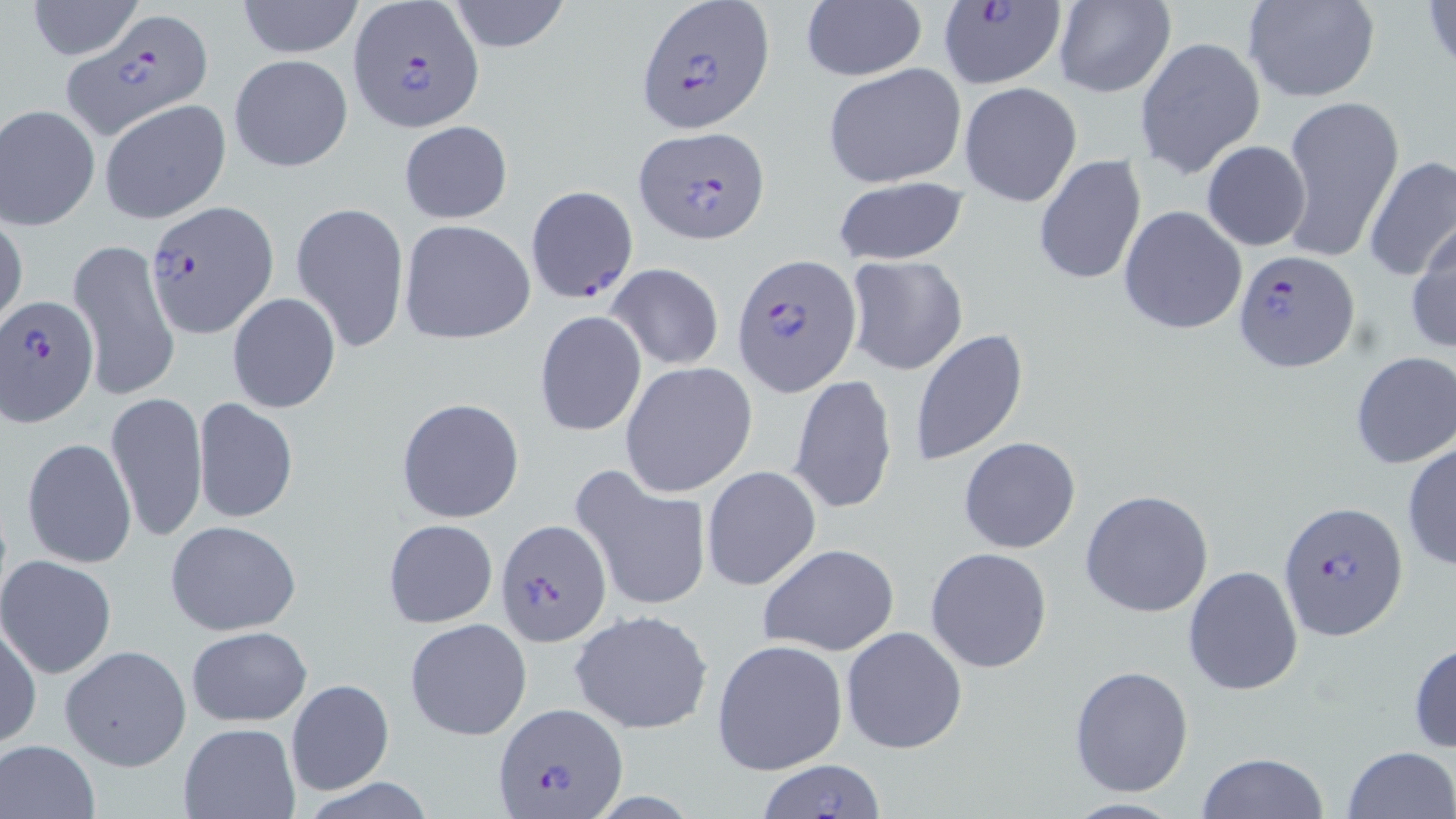

Plasmodium falciparum-infected red blood cell locations (subset) = approximate bounding boxes as [x1, y1, x2, y2] in pixels: [638, 0, 772, 131], [935, 1, 1064, 89], [350, 2, 484, 131], [62, 10, 215, 139], [634, 127, 770, 243], [525, 186, 637, 304], [145, 200, 280, 339], [1235, 250, 1357, 371], [732, 252, 864, 396], [2, 295, 99, 428], [1277, 501, 1407, 642], [495, 518, 610, 647], [494, 702, 628, 819]
slide-level diagnosis = Plasmodium falciparum
image size = 1456×819 pixels
preparation = thin blood film
magnification = 1000x
stain = May-Grünwald-Giemsa
field of view = single
uninfected red blood cell locations (subset) = approximate bounding boxes as [x1, y1, x2, y2] in pixels: [235, 0, 366, 58], [447, 0, 571, 51], [1052, 0, 1176, 97], [1242, 0, 1380, 103], [1424, 0, 1455, 78], [25, 1, 144, 59], [800, 2, 927, 82], [1135, 36, 1265, 181], [230, 54, 353, 171], [823, 62, 969, 188], [959, 82, 1083, 207], [1280, 96, 1403, 266], [0, 104, 100, 230], [398, 121, 513, 224], [1201, 140, 1311, 251], [1033, 153, 1146, 288], [1362, 154, 1455, 281], [832, 178, 970, 265], [290, 201, 409, 352], [1119, 204, 1248, 335], [1, 218, 27, 328], [398, 220, 536, 344], [1407, 220, 1456, 356], [68, 238, 180, 402], [845, 255, 968, 377], [605, 264, 725, 368], [227, 292, 341, 414], [534, 310, 647, 436], [912, 330, 1029, 467], [1350, 351, 1456, 468], [620, 363, 758, 497], [789, 374, 898, 515], [106, 391, 209, 543], [190, 396, 299, 526], [396, 397, 525, 523], [22, 437, 137, 568], [958, 437, 1081, 555], [1402, 441, 1456, 570], [701, 465, 823, 592], [572, 466, 712, 615], [1080, 490, 1214, 617], [384, 519, 497, 629], [165, 520, 302, 636], [757, 543, 900, 657], [925, 548, 1052, 672], [0, 555, 118, 679], [1182, 565, 1304, 696], [568, 608, 715, 736], [404, 617, 532, 742], [1, 618, 40, 750], [185, 626, 312, 727], [841, 626, 968, 755], [712, 638, 848, 775], [1409, 640, 1456, 755], [60, 644, 193, 772], [1069, 664, 1195, 798], [286, 678, 394, 794], [178, 723, 300, 818], [1, 738, 101, 819], [1340, 745, 1454, 819], [1193, 752, 1329, 819], [757, 759, 887, 818]
modality = light microscopy